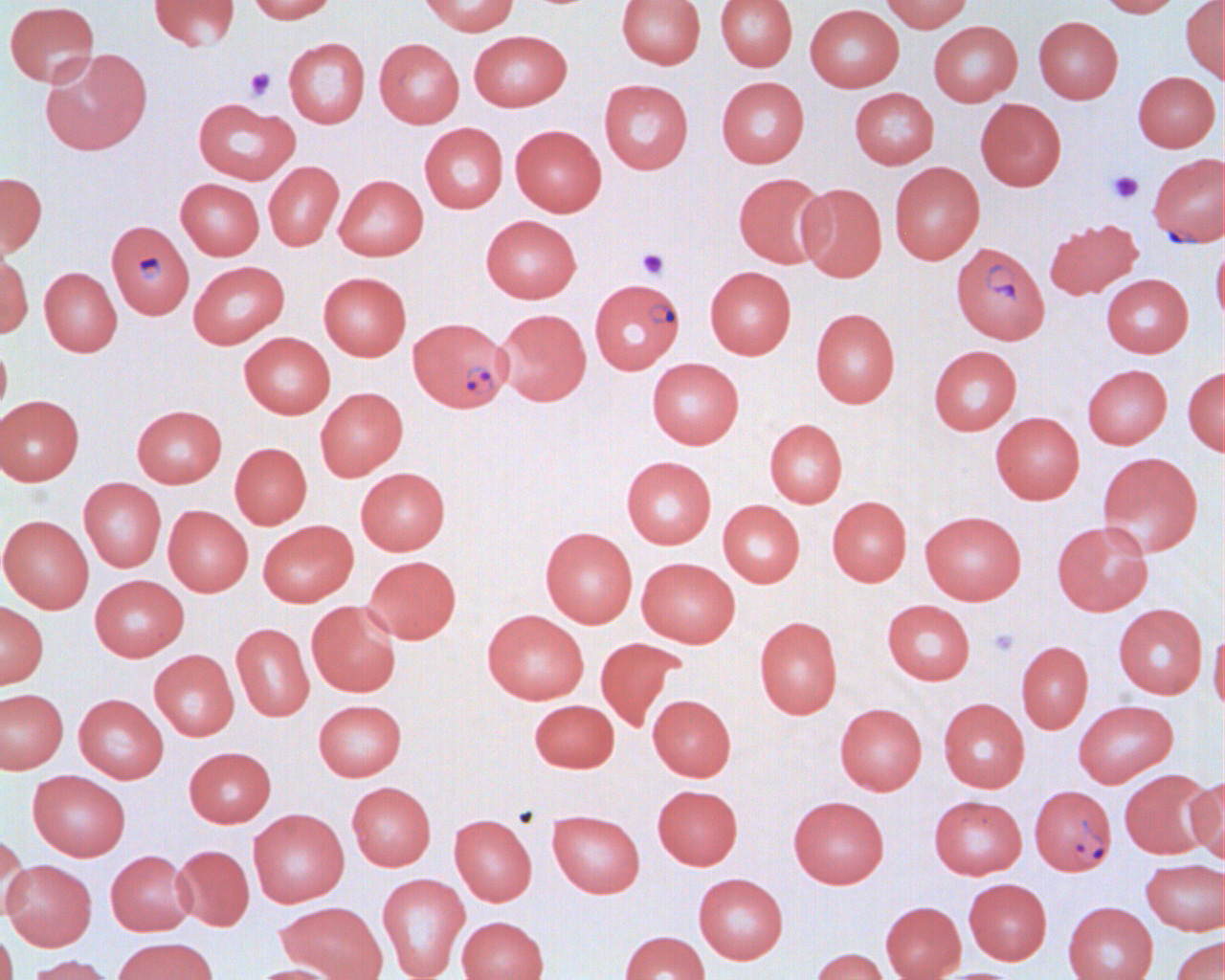

Summary:
  - Coordinate format: approximate bounding boxes as [x1, y1, x2, y2] in pixels
  - Plasmodium falciparum-infected red blood cell locations: [1148, 152, 1225, 247], [106, 220, 194, 318], [951, 242, 1050, 344], [593, 279, 687, 375], [408, 316, 512, 412], [1030, 785, 1117, 875]
  - Uninfected red blood cell locations: [149, 0, 240, 51], [247, 0, 337, 23], [418, 0, 519, 36], [617, 0, 705, 68], [716, 0, 797, 71], [879, 0, 973, 33], [1096, 0, 1184, 17], [4, 1, 99, 86], [1180, 1, 1224, 83], [804, 4, 904, 92], [1033, 16, 1123, 104], [928, 20, 1022, 106], [468, 30, 572, 112], [284, 37, 370, 128], [374, 38, 464, 127], [39, 48, 152, 155], [1132, 71, 1220, 152], [716, 76, 809, 167], [599, 79, 694, 174], [849, 87, 939, 169], [193, 97, 300, 184], [975, 98, 1067, 191], [419, 123, 508, 213], [510, 124, 606, 216], [264, 161, 344, 250], [889, 162, 985, 264], [0, 172, 47, 256], [733, 172, 831, 268], [334, 175, 428, 260], [176, 178, 264, 260], [796, 183, 887, 282], [481, 214, 581, 303], [1044, 218, 1143, 300], [1211, 238, 1225, 327], [0, 251, 33, 337], [188, 260, 289, 349], [38, 266, 122, 356], [705, 266, 796, 359], [318, 272, 411, 360], [1101, 274, 1193, 358], [495, 308, 591, 405], [810, 308, 900, 407], [239, 332, 335, 419], [0, 339, 12, 422], [928, 345, 1022, 435], [647, 357, 744, 449], [1082, 364, 1172, 449], [1183, 365, 1225, 456], [315, 387, 408, 480], [0, 395, 84, 486], [132, 405, 227, 488], [990, 412, 1085, 504], [764, 419, 847, 508], [230, 442, 312, 529], [1097, 452, 1203, 557], [621, 456, 717, 549], [355, 467, 450, 555], [79, 477, 166, 572], [827, 496, 911, 586], [718, 500, 805, 587], [163, 505, 253, 596], [920, 510, 1026, 604], [0, 515, 94, 613], [258, 520, 358, 607], [1052, 520, 1153, 616], [540, 526, 637, 627], [363, 555, 461, 643], [636, 557, 740, 647], [89, 574, 189, 661], [0, 599, 48, 689], [882, 599, 975, 685], [306, 600, 402, 697], [1113, 604, 1208, 698], [482, 610, 588, 704], [754, 616, 842, 719], [231, 623, 314, 721], [1208, 628, 1225, 717], [595, 637, 685, 731], [1016, 641, 1093, 733], [149, 650, 239, 740], [0, 689, 68, 773], [73, 694, 168, 783], [648, 694, 735, 781], [938, 698, 1030, 792], [313, 699, 406, 781], [529, 699, 619, 772], [1073, 700, 1178, 788], [834, 703, 927, 795], [184, 746, 276, 827], [1118, 769, 1218, 859], [28, 770, 130, 861], [1188, 776, 1225, 863], [346, 781, 436, 870], [652, 784, 743, 870], [929, 795, 1027, 879], [788, 796, 889, 888], [248, 809, 349, 907], [547, 810, 645, 897], [449, 814, 537, 905], [0, 831, 31, 920], [173, 844, 254, 931], [105, 850, 196, 936], [1141, 858, 1225, 935], [1, 859, 96, 951], [377, 873, 470, 979], [693, 873, 788, 964], [963, 878, 1052, 965], [276, 901, 388, 980], [880, 901, 966, 980], [1063, 901, 1158, 980], [456, 915, 550, 980], [0, 926, 18, 980], [619, 931, 710, 980], [1170, 935, 1224, 980], [111, 936, 218, 980], [811, 948, 889, 980], [25, 954, 118, 980], [244, 964, 343, 980], [931, 967, 1025, 980]
  - Platelet locations: [244, 67, 276, 101], [1107, 170, 1144, 204], [637, 248, 669, 279], [988, 627, 1019, 657]
  - Slide-level diagnosis: Plasmodium falciparum
  - Image size: 1225×980 pixels
  - Modality: light microscopy
  - Field of view: single
  - Preparation: thin blood film
  - Magnification: 1000x